Give the position of every Plasmodium falciparum parasite, noting its life-cycle stage.
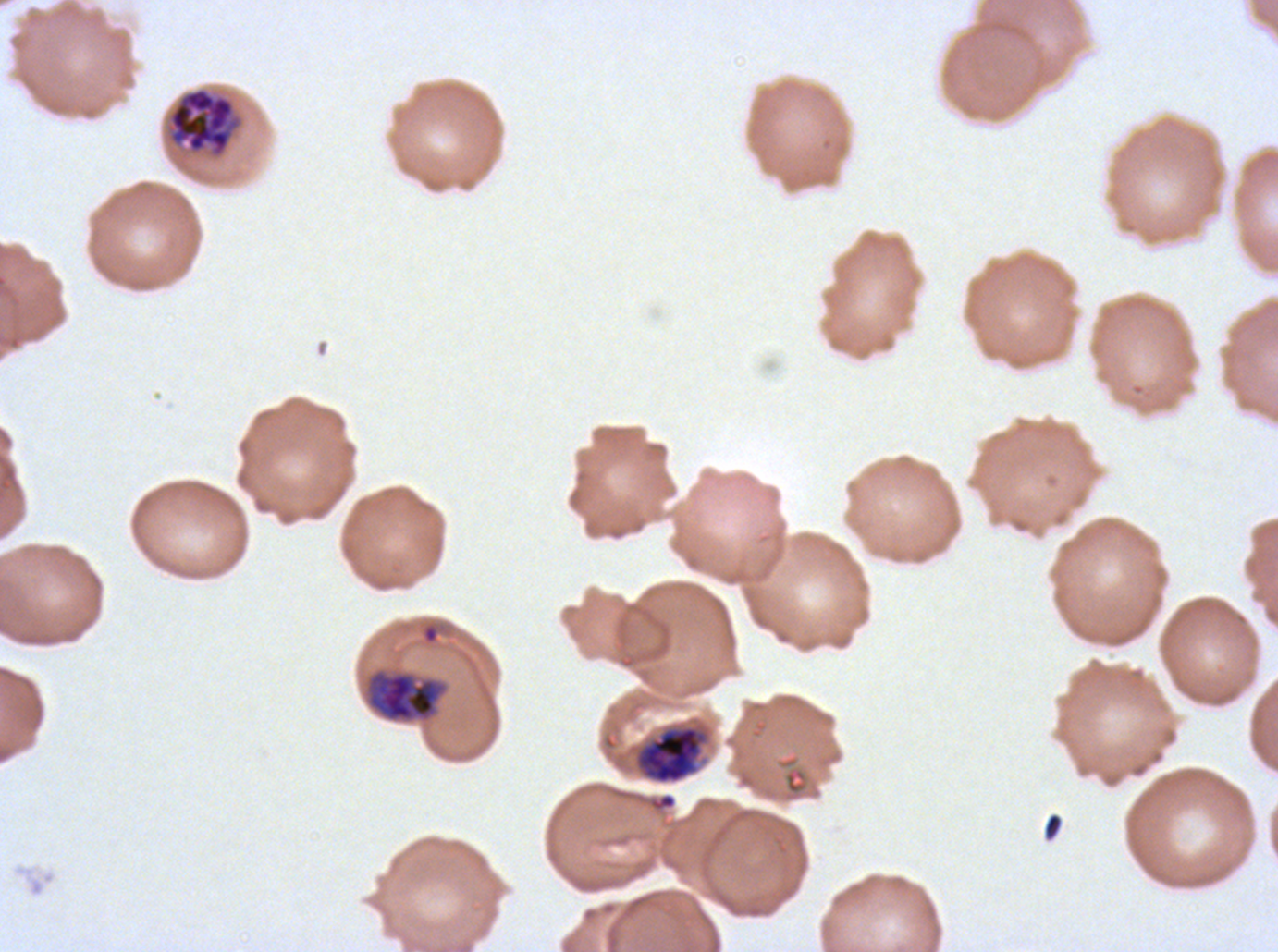
Approximate bounding rectangles given as corner coordinates in pixels from the top-left.
Early schizonts: (x1=365, y1=669, x2=447, y2=723), (x1=634, y1=725, x2=707, y2=785).
Late schizonts: (x1=169, y1=89, x2=234, y2=153).
No rings, late-ring/early-trophozoite forms, mid trophozoites, late trophozoites, segmenters, or gametocytes observed.

debris locations = (x1=1042, y1=812, x2=1064, y2=843)
preparation = thin blood smear
stain = Giemsa
image size = 1278×952 pixels
specimen = Plasmodium falciparum from a patient in The Gambia, cultured ex vivo for 24 to 48 hours
field of view = sub-image separated from a larger composite
life-cycle stages observed = early schizont, late schizont